Assess this cell for malaria.
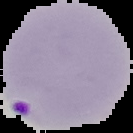
It is parasitized.

Cell region segmented out of the field of view; the surrounding area is masked to black. From a thin blood smear. Image is 133×133 pixels.